State which parasite is depicted.
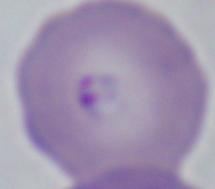

Babesia.

modality = photomicrograph
magnification = 1000x